Report the malaria status of this cell.
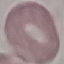
It is uninfected.

Summary:
  - Preparation: thin blood smear
  - Capture: smartphone camera at the microscope eyepiece
  - Stain: Giemsa
  - Image type: cell patch, automatically extracted from a larger field of view and resized to 64 × 64 pixels